Report the malaria status of this cell.
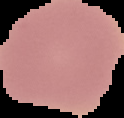

It is uninfected.

{
  "preparation": "thin blood film",
  "image_size": "124×118 pixels",
  "image_type": "segmented cell region on a black background"
}